Comment on the morphology of the red blood cells.
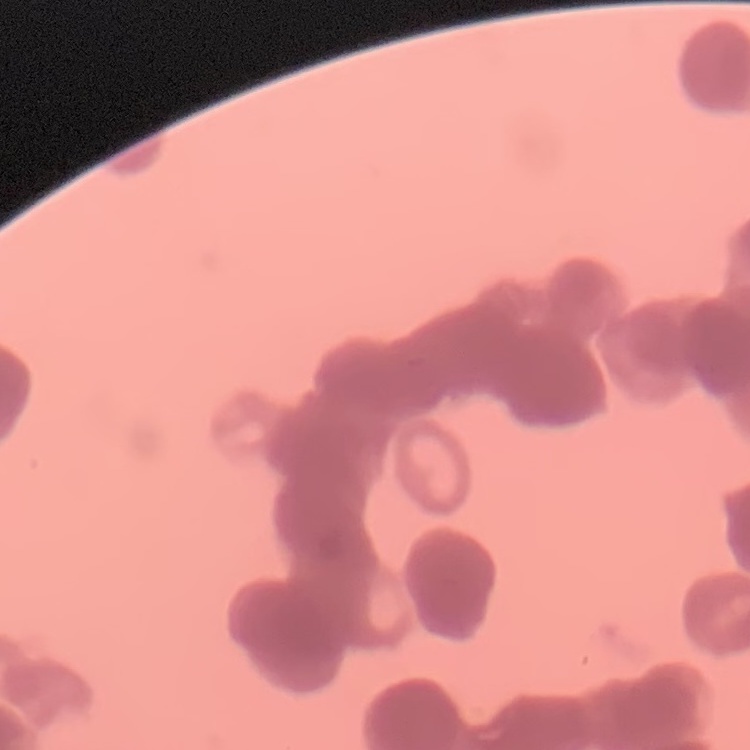

They show rouleaux formation.

Summary:
  - Stain: Field's or Giemsa
  - Preparation: thin blood smear
  - Image type: square crop of a larger photomicrograph